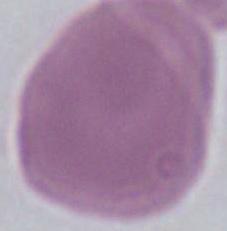

Micrograph. Captured at 1000x magnification. An erythrocyte is shown.